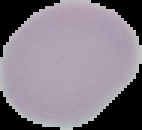

Summary:
  - Image type: segmented cell region on a black background
  - Result: negative for malaria parasites
  - Image size: 142×130 pixels
  - Preparation: thin blood smear